Locate every Plasmodium ovale-infected red blood cell.
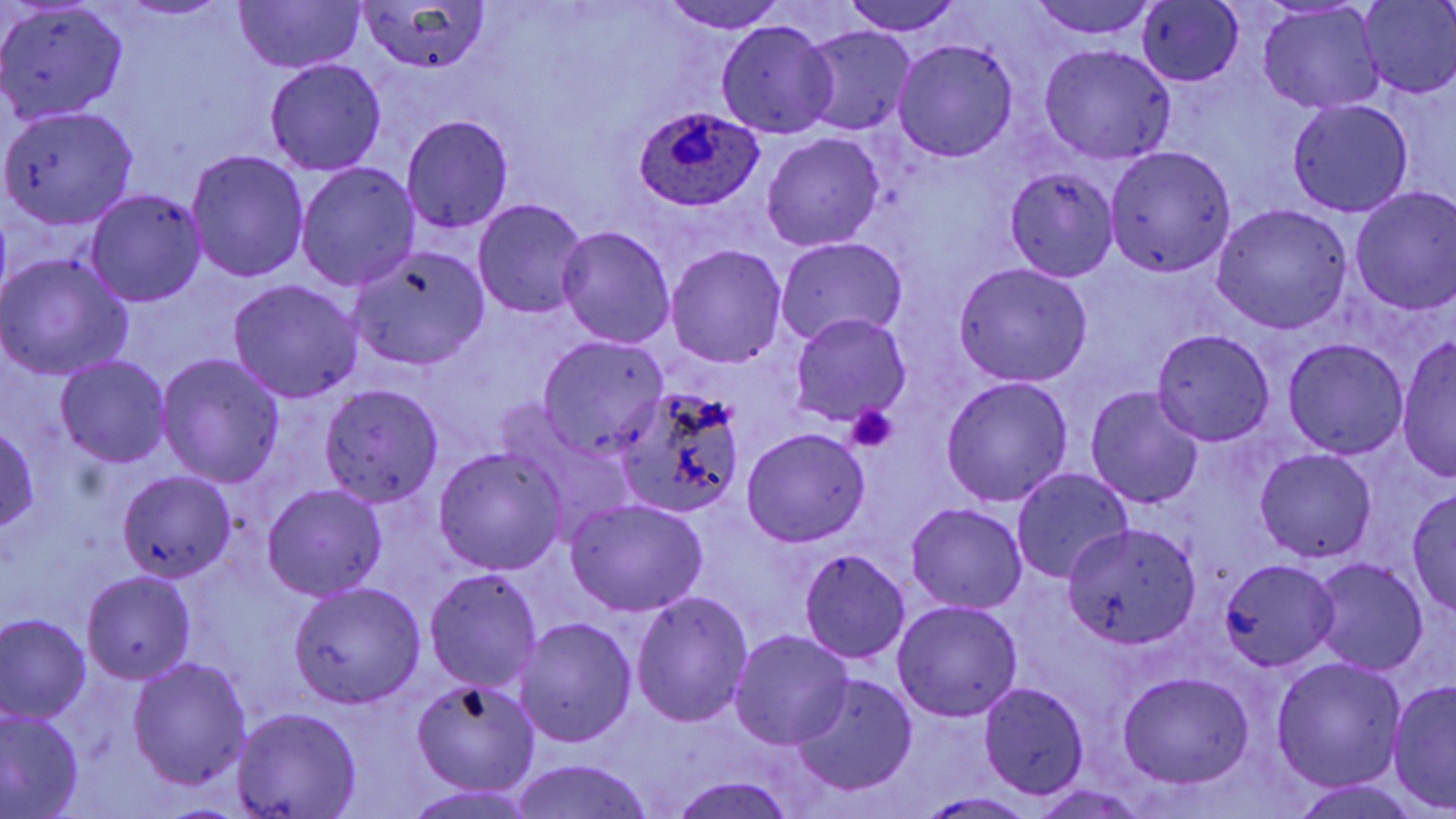

Approximate bounding boxes as (x1, y1, x2, y2) in pixels.
Plasmodium ovale-infected red blood cells: (633, 106, 765, 212).

Summary:
  - Uninfected red blood cell locations: (656, 0, 789, 33), (841, 0, 964, 36), (1025, 0, 1160, 37), (1359, 0, 1456, 98), (233, 1, 366, 72), (0, 2, 129, 123), (355, 2, 491, 74), (1137, 2, 1244, 87), (1257, 5, 1386, 114), (715, 20, 838, 140), (802, 27, 917, 135), (893, 40, 1018, 162), (1037, 45, 1175, 163), (264, 59, 387, 176), (1288, 98, 1413, 216), (2, 104, 137, 229), (400, 115, 514, 235), (762, 133, 884, 250), (1105, 146, 1237, 276), (186, 150, 309, 282), (296, 162, 420, 290), (1006, 167, 1120, 281), (1349, 187, 1456, 314), (86, 189, 206, 307), (472, 199, 591, 318), (1212, 205, 1353, 334), (556, 226, 677, 349), (775, 236, 908, 348), (665, 245, 787, 367), (347, 247, 491, 373), (0, 253, 133, 380), (954, 263, 1092, 387), (228, 279, 364, 403), (787, 313, 911, 428), (1152, 329, 1275, 445), (1396, 336, 1456, 480), (538, 337, 671, 457), (1283, 339, 1409, 458), (157, 353, 284, 486), (55, 354, 172, 467), (941, 376, 1074, 507), (320, 384, 444, 506), (1084, 386, 1206, 509), (614, 389, 745, 524), (0, 426, 41, 532), (742, 428, 871, 547), (433, 447, 567, 575), (1254, 448, 1376, 564), (1010, 468, 1135, 584), (119, 472, 236, 583), (263, 483, 387, 602), (1407, 489, 1455, 614), (564, 498, 708, 617), (906, 502, 1028, 614), (1064, 520, 1201, 648), (798, 548, 911, 663), (1309, 559, 1428, 675), (1218, 560, 1340, 670), (423, 568, 543, 692), (82, 571, 196, 683), (289, 581, 425, 708), (629, 591, 754, 730), (891, 600, 1023, 722), (1, 615, 92, 723), (513, 617, 637, 748), (730, 630, 853, 750), (1270, 656, 1406, 793), (128, 657, 252, 791), (1117, 671, 1255, 788), (793, 673, 918, 796), (409, 676, 541, 797), (1386, 680, 1456, 814), (978, 682, 1088, 799), (233, 706, 361, 818), (0, 708, 83, 817), (509, 759, 656, 819), (667, 773, 801, 819), (1027, 783, 1150, 819), (402, 787, 543, 818), (915, 792, 1041, 819)
  - Platelet locations: (845, 404, 899, 455)
  - Slide-level diagnosis: Plasmodium ovale
  - Modality: light microscopy
  - Magnification: 1000x
  - Stain: May-Grünwald-Giemsa
  - Image size: 1456×819 pixels
  - Field of view: single
  - Preparation: thin blood film